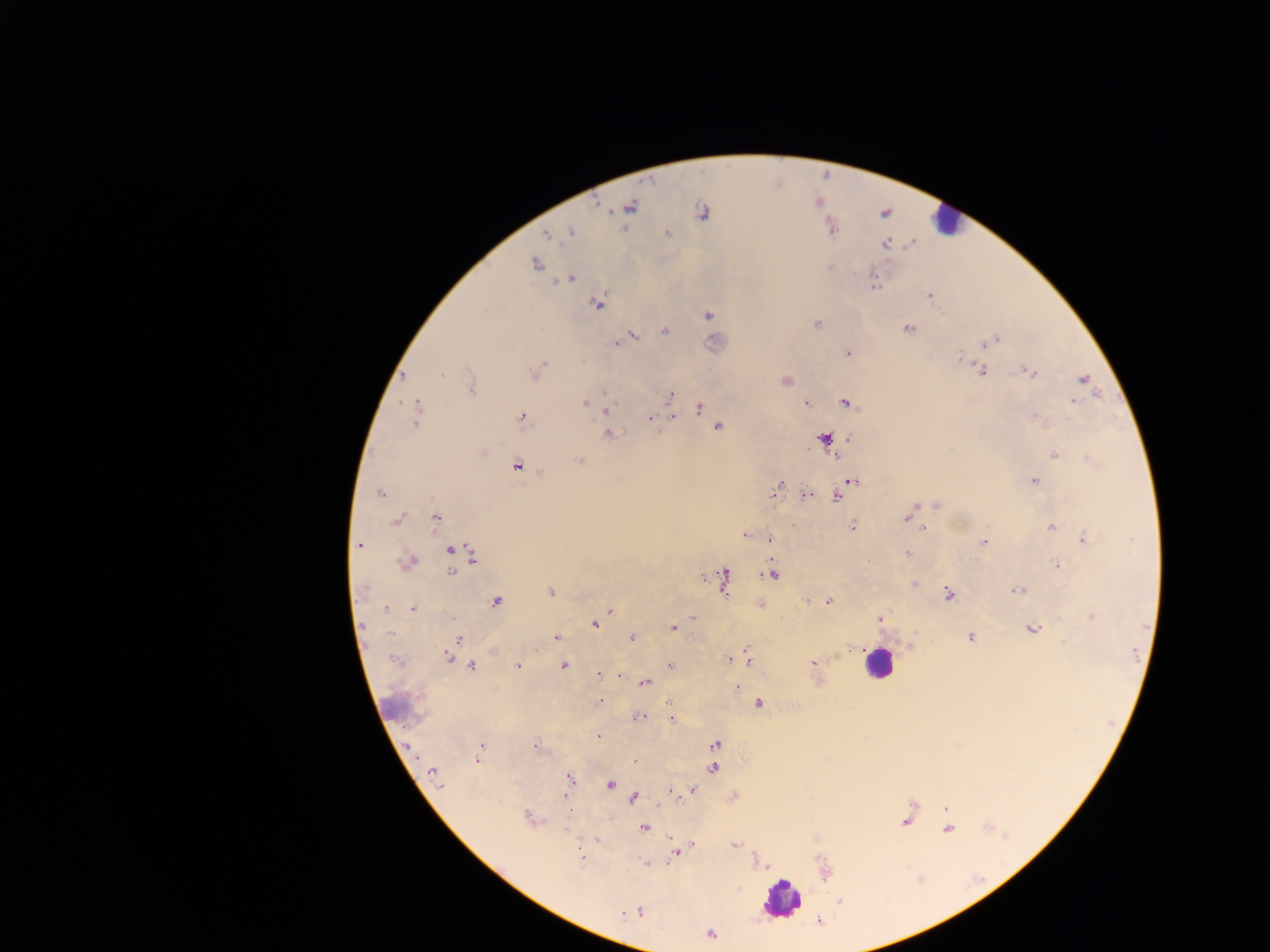
Approximate centers as [x, y] in pixels.
Summary:
  - Leukocyte locations: [945, 220], [824, 439], [877, 662], [397, 707], [782, 900]
  - Malaria parasite locations: [630, 206], [702, 212], [571, 232], [667, 233], [547, 234], [886, 243], [535, 264], [830, 267], [570, 279], [874, 286], [930, 295], [597, 304], [484, 310], [709, 315], [817, 324], [908, 328], [664, 330], [631, 336], [997, 339], [618, 342], [984, 345], [847, 353], [959, 358], [543, 364], [982, 370], [1030, 372], [535, 373], [441, 374], [403, 375], [1083, 379], [785, 381], [470, 388], [606, 392], [671, 394], [1073, 400], [584, 403], [806, 403], [846, 403], [606, 406], [699, 408], [416, 411], [522, 417], [1036, 417], [650, 418], [673, 418], [718, 427], [609, 434], [483, 452], [1055, 454], [835, 455], [580, 461], [517, 466], [1035, 481], [853, 482], [777, 487], [380, 493], [806, 495], [838, 496], [937, 506], [914, 509], [436, 517], [908, 517], [397, 520], [852, 526], [1051, 527], [922, 529], [745, 536], [769, 539], [1084, 540], [985, 542], [359, 545], [449, 550], [906, 553], [473, 557], [408, 562], [1057, 565], [451, 572], [772, 574], [724, 578], [361, 589], [1017, 590], [550, 591], [948, 594], [496, 601], [808, 601], [829, 602], [761, 605], [385, 609], [412, 609], [609, 611], [692, 617], [1091, 617], [881, 619], [595, 624], [673, 628], [1032, 628], [391, 633], [556, 637], [970, 637], [459, 638], [632, 638], [494, 652], [447, 657], [748, 657], [394, 659], [728, 660], [813, 663], [517, 666], [563, 666], [670, 666], [472, 667], [599, 674], [620, 676], [645, 683], [736, 688], [600, 701], [759, 703], [638, 718], [671, 719], [598, 737], [715, 745], [482, 746], [535, 747], [479, 752], [478, 760], [634, 762], [713, 769], [433, 771], [569, 779], [609, 785], [440, 787], [692, 790], [672, 792], [566, 794], [634, 798], [946, 809], [529, 817], [905, 822], [643, 828], [948, 829], [597, 840], [693, 845], [735, 846], [676, 853], [582, 857], [645, 862], [639, 912], [622, 913], [711, 935]
  - Image size: 1270×952 pixels
  - Capture: mobile-phone photograph through a microscope
  - Field of view: single
  - Preparation: thick blood film
  - Country: Ghana